Report the malaria status of this cell.
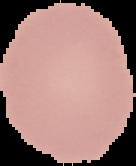
It is uninfected.

The area outside the segmented cell region is set to black. Image is 136×166 pixels. From a thin blood smear.